Locate and identify every blood parasite.
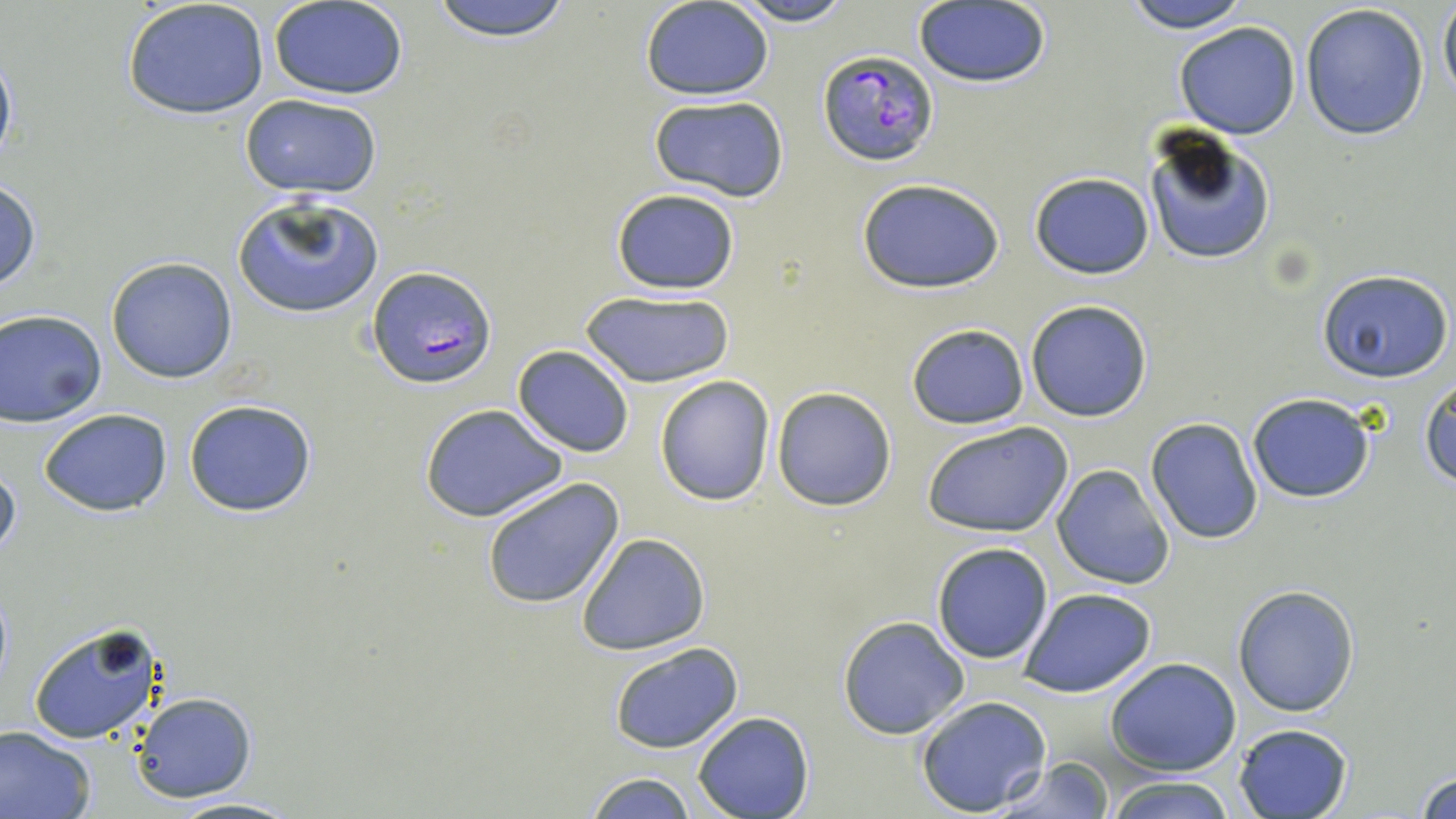
Approximate bounding boxes as named x1/y1/x2/y2 corners in pixels.
Plasmodium falciparum-infected red blood cells: (x1=818, y1=50, x2=940, y2=166), (x1=367, y1=266, x2=496, y2=387).
No Plasmodium ovale, Plasmodium malariae, Plasmodium vivax, Babesia divergens, or Trypanosoma brucei observed.

Uninfected red blood cell locations: (x1=122, y1=0, x2=270, y2=121), (x1=427, y1=0, x2=576, y2=42), (x1=725, y1=0, x2=857, y2=26), (x1=1117, y1=0, x2=1256, y2=32), (x1=1438, y1=0, x2=1456, y2=108), (x1=269, y1=2, x2=409, y2=99), (x1=641, y1=2, x2=773, y2=100), (x1=914, y1=3, x2=1050, y2=88), (x1=1299, y1=3, x2=1432, y2=142), (x1=1173, y1=21, x2=1303, y2=140), (x1=0, y1=42, x2=17, y2=176), (x1=238, y1=94, x2=383, y2=199), (x1=646, y1=95, x2=790, y2=203), (x1=1141, y1=126, x2=1277, y2=267), (x1=1029, y1=171, x2=1155, y2=279), (x1=856, y1=178, x2=1005, y2=294), (x1=0, y1=179, x2=42, y2=294), (x1=609, y1=187, x2=741, y2=295), (x1=232, y1=195, x2=384, y2=319), (x1=105, y1=256, x2=239, y2=384), (x1=1316, y1=269, x2=1452, y2=382), (x1=579, y1=290, x2=734, y2=387), (x1=1025, y1=299, x2=1153, y2=422), (x1=1, y1=310, x2=107, y2=426), (x1=905, y1=323, x2=1029, y2=429), (x1=513, y1=345, x2=634, y2=457), (x1=655, y1=376, x2=775, y2=506), (x1=1421, y1=376, x2=1456, y2=488), (x1=771, y1=386, x2=898, y2=512), (x1=1246, y1=392, x2=1377, y2=503), (x1=183, y1=398, x2=319, y2=518), (x1=420, y1=402, x2=570, y2=523), (x1=39, y1=407, x2=173, y2=517), (x1=1144, y1=417, x2=1264, y2=545), (x1=920, y1=421, x2=1075, y2=539), (x1=0, y1=461, x2=21, y2=570), (x1=1051, y1=464, x2=1175, y2=590), (x1=479, y1=476, x2=627, y2=611), (x1=577, y1=532, x2=711, y2=656), (x1=930, y1=542, x2=1054, y2=665), (x1=1232, y1=585, x2=1360, y2=716), (x1=1019, y1=587, x2=1157, y2=697), (x1=837, y1=616, x2=970, y2=739), (x1=28, y1=624, x2=166, y2=745), (x1=607, y1=641, x2=745, y2=753), (x1=1105, y1=657, x2=1242, y2=773), (x1=130, y1=692, x2=257, y2=804), (x1=914, y1=695, x2=1052, y2=816), (x1=692, y1=712, x2=814, y2=819), (x1=1233, y1=723, x2=1353, y2=818), (x1=0, y1=726, x2=98, y2=819), (x1=989, y1=756, x2=1115, y2=818), (x1=1414, y1=764, x2=1456, y2=819), (x1=579, y1=772, x2=701, y2=818), (x1=1105, y1=776, x2=1239, y2=819), (x1=164, y1=795, x2=304, y2=818). Slide-level diagnosis: Plasmodium falciparum. May-Grünwald-Giemsa stain. Image is 1456×819 pixels. Optical microscopy. 1000x magnification. Thin blood film. Single field of view.